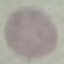

Malaria status: uninfected. Thin blood film. Acquired by smartphone through the microscope eyepiece. Cell patch, automatically extracted from a larger field of view and resized to 64 × 64 pixels. Giemsa stain.